Classify this cell by malaria status.
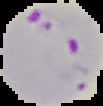
It is parasitized.

preparation = thin blood film
image size = 103×106 pixels
image type = segmented cell region on a black background